Locate every Plasmodium parasite.
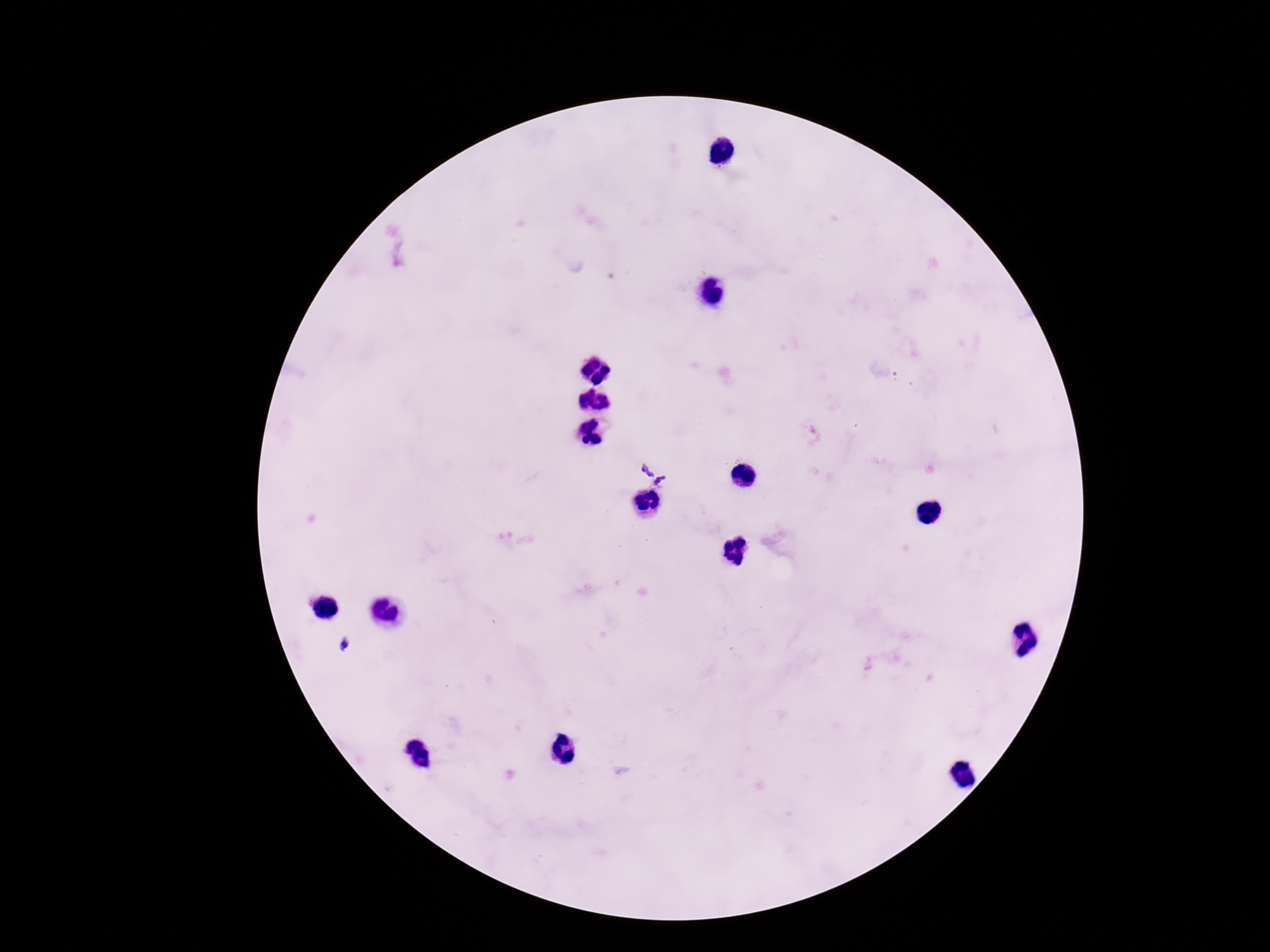

Approximate centers as [x, y] in pixels.
Plasmodium parasites: [651, 468], [662, 483], [344, 644].

Summary:
  - Stain: Giemsa
  - Patient malaria status: infected
  - Preparation: thick peripheral-blood smear
  - Image size: 1270×952 pixels
  - Field of view: one from this slide
  - Magnification: 100x
  - Capture: smartphone camera through the microscope eyepiece